Identify the blood parasite species.
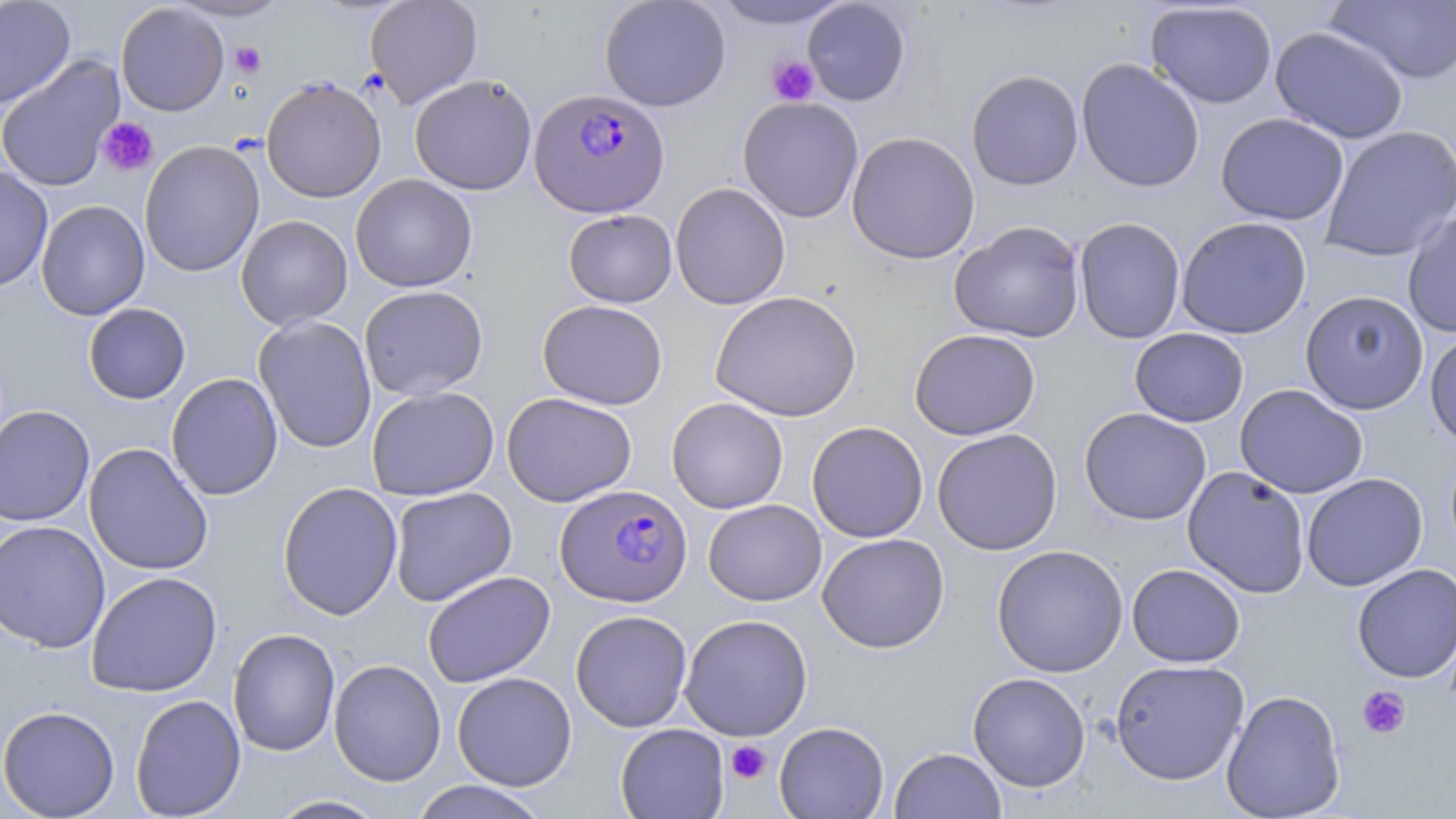

Plasmodium falciparum.

{
  "uninfected_red_blood_cell_locations": "approximate bounding boxes as (x1, y1, x2, y2) in pixels: (0, 0, 76, 109), (167, 0, 293, 21), (365, 0, 483, 108), (599, 0, 731, 112), (708, 0, 856, 30), (802, 0, 911, 106), (1325, 0, 1456, 85), (115, 2, 229, 116), (1144, 2, 1278, 109), (1270, 26, 1409, 144), (0, 56, 124, 192), (1076, 57, 1205, 192), (966, 69, 1084, 191), (409, 74, 537, 195), (261, 77, 386, 203), (737, 96, 864, 223), (1214, 112, 1349, 225), (1320, 125, 1456, 263), (846, 131, 980, 264), (139, 140, 264, 277), (0, 164, 53, 293), (350, 174, 477, 293), (669, 182, 791, 310), (36, 200, 150, 321), (564, 209, 677, 308), (1402, 210, 1456, 338), (236, 214, 353, 331), (1175, 216, 1312, 339), (1075, 217, 1186, 345), (949, 221, 1085, 343), (359, 285, 488, 401), (710, 290, 862, 422), (1300, 290, 1429, 415), (537, 299, 668, 410), (83, 303, 191, 404), (253, 315, 377, 453), (909, 328, 1041, 440), (1129, 328, 1249, 427), (1425, 328, 1456, 452), (166, 373, 283, 501), (1234, 384, 1368, 499), (366, 386, 499, 501), (501, 392, 637, 507), (666, 397, 788, 514), (0, 405, 94, 526), (1079, 407, 1212, 525), (806, 421, 929, 543), (932, 428, 1063, 555), (84, 442, 213, 575), (1182, 466, 1310, 598), (1301, 473, 1427, 592), (277, 481, 403, 620), (389, 487, 517, 606), (703, 499, 827, 606), (0, 520, 111, 653), (817, 533, 950, 653), (991, 544, 1128, 678), (1126, 563, 1245, 668), (1352, 564, 1456, 683), (85, 571, 223, 697), (423, 571, 555, 688), (570, 610, 692, 732), (679, 614, 813, 740), (228, 628, 340, 757), (329, 658, 446, 787), (1110, 659, 1250, 785), (452, 671, 577, 791), (968, 672, 1090, 792), (1221, 689, 1346, 818), (130, 694, 246, 818), (0, 705, 120, 818), (774, 721, 889, 818), (614, 724, 729, 818), (889, 747, 1006, 819), (409, 781, 551, 818), (266, 795, 389, 818)",
  "plasmodium_falciparum_infected_red_blood_cell_locations": "approximate bounding boxes as (x1, y1, x2, y2) in pixels: (529, 87, 668, 218), (553, 489, 691, 612)",
  "field_of_view": "single",
  "magnification": "1000x",
  "platelet_locations": "approximate bounding boxes as (x1, y1, x2, y2) in pixels: (230, 41, 266, 78), (767, 56, 819, 106), (97, 117, 158, 177), (1356, 686, 1411, 739), (725, 740, 772, 784)",
  "preparation": "thin blood film",
  "modality": "optical microscopy",
  "image_size": "1456×819 pixels",
  "stain": "May-Grünwald-Giemsa"
}